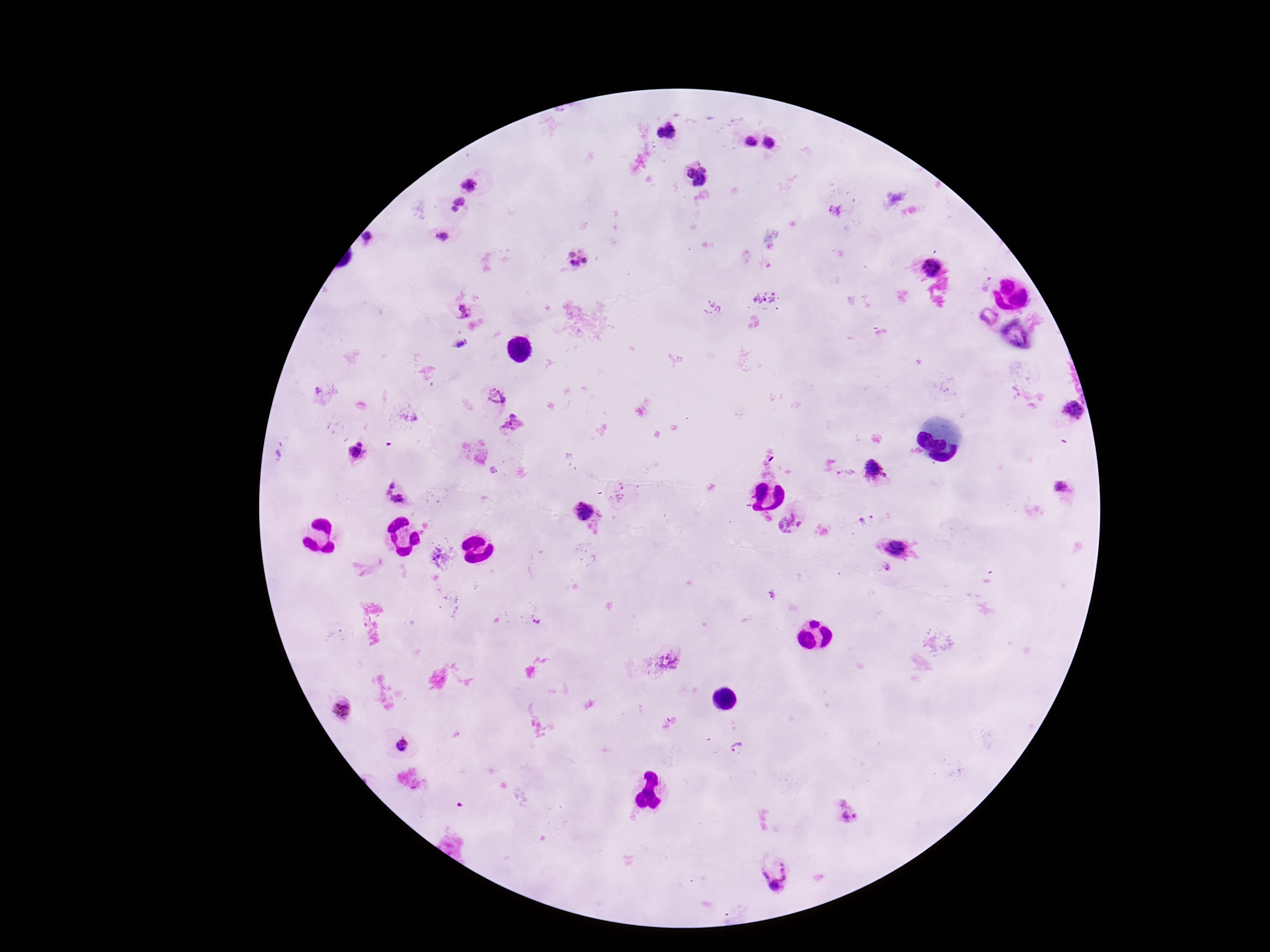

Approximate object centers, in pixels from the top-left corner.
Summary:
  - Plasmodium parasite locations: (x=667, y=133), (x=748, y=143), (x=770, y=144), (x=696, y=176), (x=471, y=184), (x=458, y=203), (x=833, y=212), (x=441, y=235), (x=579, y=261), (x=932, y=268), (x=766, y=300), (x=713, y=308), (x=459, y=311), (x=988, y=317), (x=461, y=344), (x=497, y=394), (x=1076, y=411), (x=513, y=424), (x=357, y=450), (x=875, y=471), (x=848, y=474), (x=1061, y=489), (x=396, y=493), (x=581, y=511), (x=868, y=520), (x=792, y=523), (x=897, y=549), (x=441, y=557), (x=886, y=569), (x=535, y=622), (x=668, y=661), (x=342, y=708), (x=402, y=745), (x=738, y=750), (x=847, y=814), (x=776, y=876)
  - Field of view: one from this slide
  - Stain: Giemsa
  - Image size: 1270×952 pixels
  - Capture: smartphone camera through the microscope eyepiece
  - Patient malaria status: infected
  - Preparation: thick peripheral-blood smear
  - Magnification: 100x